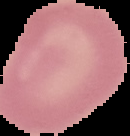
Summary:
  - Image type: segmented cell region on a black background
  - Image size: 130×136 pixels
  - Preparation: thin blood film
  - Result: no Plasmodium parasites seen